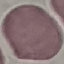

malaria_status: uninfected
image_type: cell patch, automatically extracted from a larger field of view and resized to 64 × 64 pixels
capture: smartphone camera at the microscope eyepiece
preparation: thin blood film
stain: Giemsa